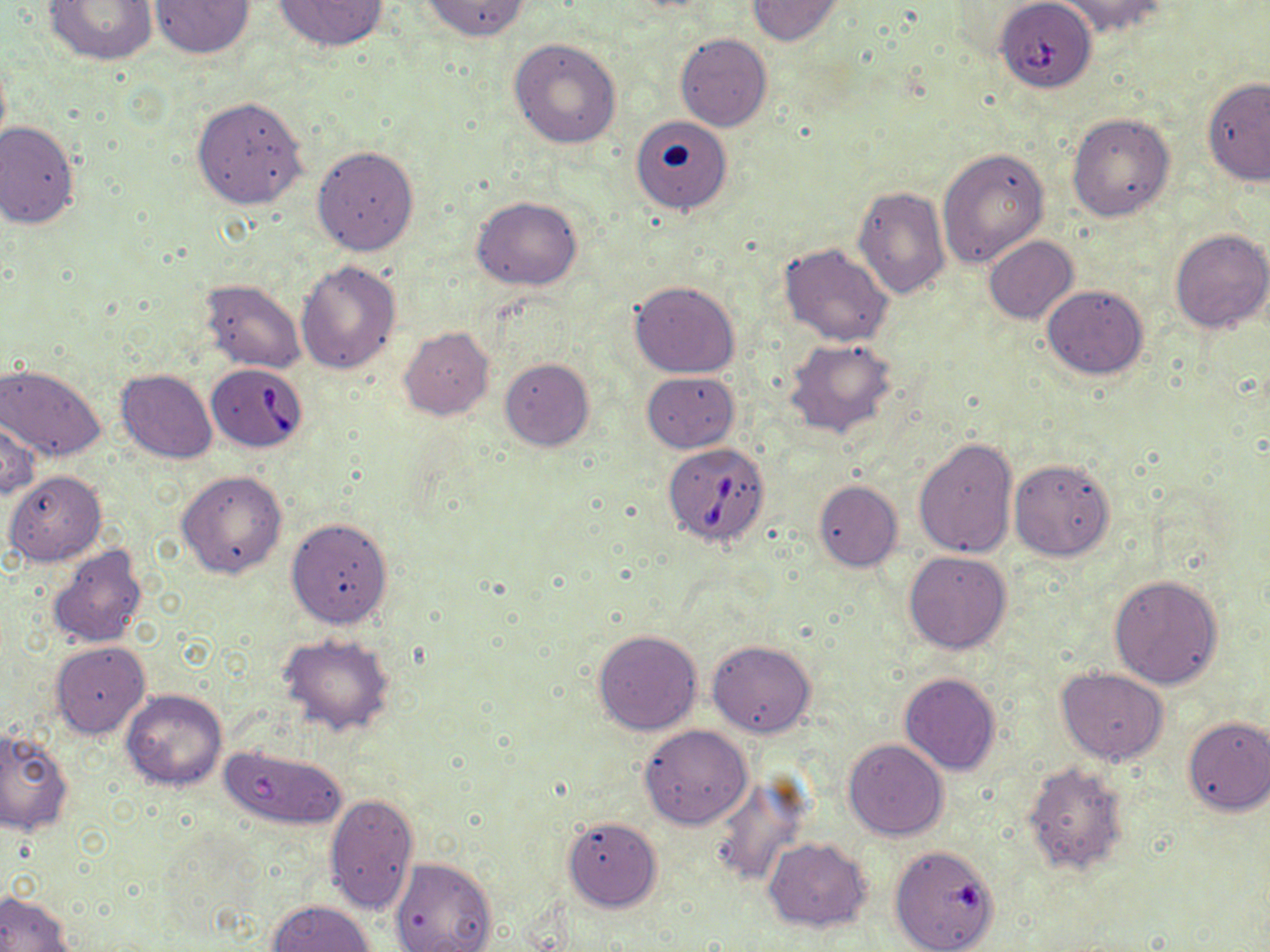

{
  "slide_level_diagnosis": "Babesia divergens",
  "stain": "May-Grünwald-Giemsa",
  "babesia_divergens_infected_red_blood_cell_locations": "approximate bounding boxes as (x1, y1, x2, y2) in pixels: (998, 3, 1092, 91), (206, 361, 310, 452), (662, 442, 771, 548)",
  "image_size": "1270×952 pixels",
  "magnification": "1000x",
  "field_of_view": "single",
  "preparation": "thin blood smear",
  "uninfected_red_blood_cell_locations": "approximate bounding boxes as (x1, y1, x2, y2) in pixels: (42, 0, 159, 66), (271, 0, 389, 52), (418, 0, 530, 41), (747, 0, 844, 45), (1055, 0, 1172, 38), (149, 1, 257, 59), (675, 33, 772, 132), (509, 37, 622, 149), (1202, 78, 1270, 185), (192, 96, 307, 211), (1066, 112, 1175, 223), (629, 113, 739, 217), (0, 121, 80, 229), (312, 144, 420, 256), (937, 146, 1049, 268), (853, 185, 950, 301), (472, 196, 583, 291), (1169, 230, 1270, 333), (983, 236, 1079, 324), (779, 242, 894, 347), (297, 260, 402, 374), (199, 280, 305, 374), (629, 281, 740, 378), (1042, 285, 1148, 380), (400, 327, 494, 421), (785, 338, 899, 439), (499, 357, 595, 450), (1, 363, 105, 460), (116, 369, 218, 464), (641, 371, 739, 452), (0, 411, 41, 502), (913, 437, 1018, 560), (1009, 457, 1116, 559), (5, 470, 107, 566), (176, 470, 287, 579), (813, 480, 903, 571), (286, 517, 393, 629), (46, 543, 149, 650), (903, 550, 1013, 654), (1108, 573, 1223, 689), (592, 629, 703, 735), (278, 633, 396, 735), (708, 640, 816, 738), (51, 642, 149, 740), (1056, 668, 1168, 764), (899, 673, 1000, 776), (120, 688, 228, 791), (1181, 715, 1270, 814), (639, 725, 752, 828), (0, 727, 74, 836), (843, 739, 948, 840), (221, 742, 349, 831), (1022, 761, 1129, 876), (709, 775, 812, 886), (324, 792, 419, 916), (562, 816, 662, 911), (763, 838, 872, 931), (895, 852, 994, 951), (389, 856, 497, 952), (0, 891, 74, 952), (267, 900, 376, 952)",
  "modality": "optical microscopy"
}